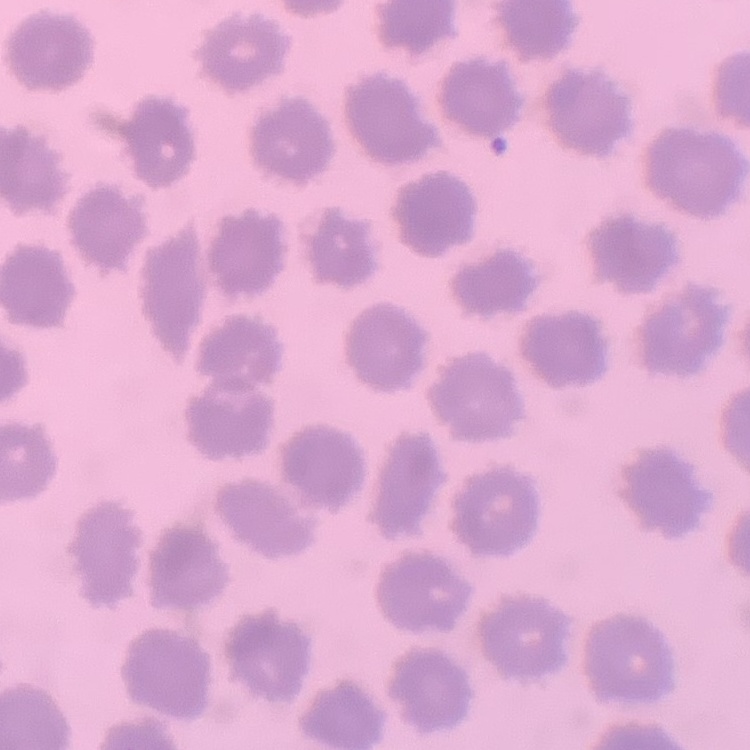 The erythrocytes exhibit no rouleaux formation. Stained with either Field's or Giemsa. Square crop of a larger photomicrograph. Thin blood film.